Outline each Babesia divergens-infected red blood cell.
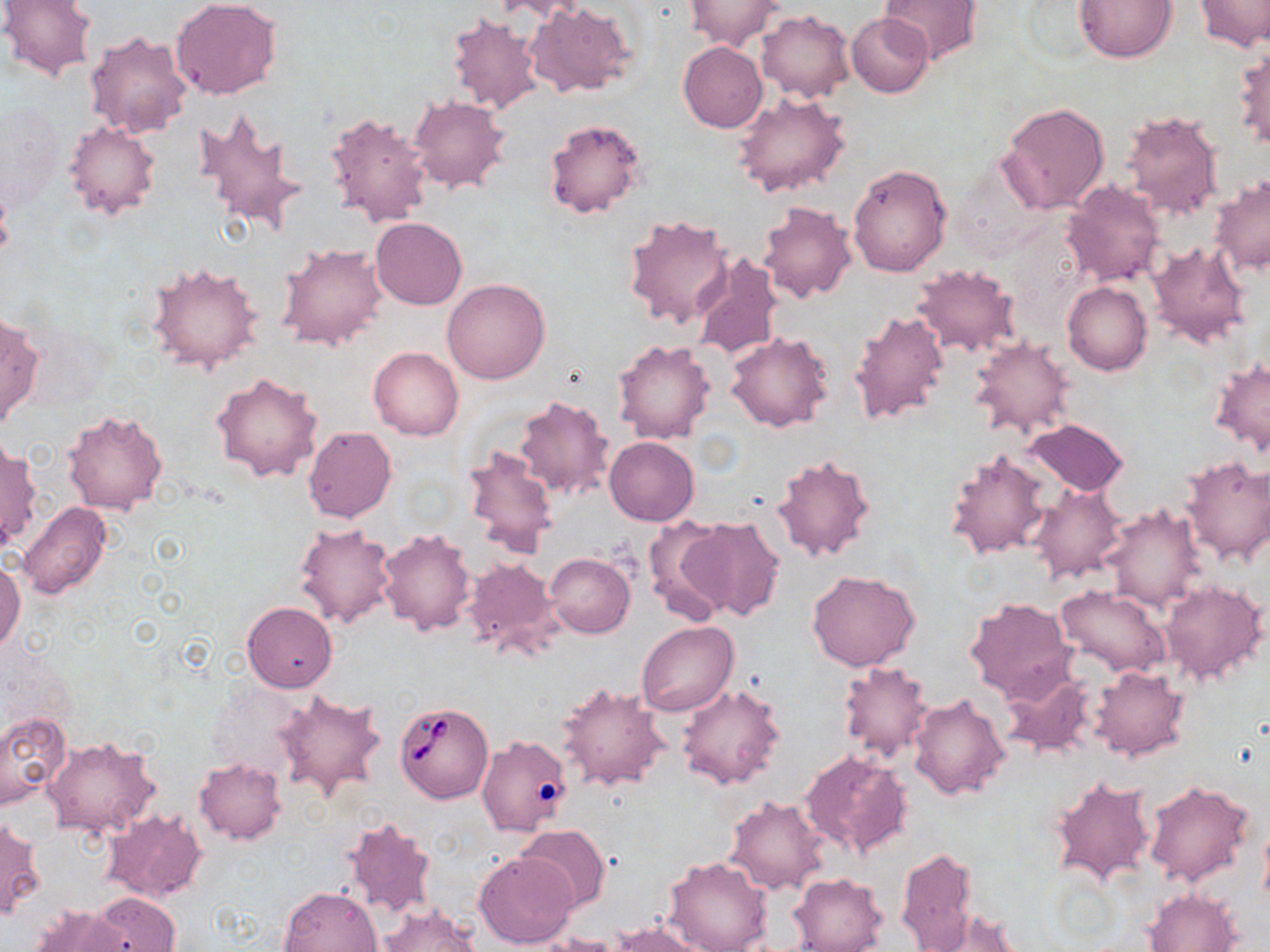

Approximate bounding boxes as [x1, y1, x2, y2] in pixels.
Babesia divergens-infected red blood cells: [394, 701, 494, 804].

Summary:
  - Uninfected red blood cell locations: [0, 0, 97, 81], [170, 0, 282, 101], [493, 0, 594, 22], [878, 0, 982, 66], [1075, 0, 1178, 63], [1195, 0, 1269, 51], [684, 1, 785, 51], [525, 3, 636, 98], [756, 10, 854, 103], [447, 13, 543, 115], [846, 13, 934, 99], [85, 32, 192, 140], [677, 41, 768, 132], [1232, 42, 1269, 151], [733, 92, 851, 197], [409, 95, 510, 193], [999, 102, 1111, 213], [194, 107, 306, 232], [323, 109, 434, 229], [1119, 110, 1224, 221], [543, 116, 648, 220], [64, 120, 161, 220], [848, 164, 952, 277], [1210, 176, 1269, 277], [1060, 180, 1166, 287], [756, 200, 858, 303], [624, 213, 734, 330], [370, 217, 467, 310], [1146, 241, 1252, 348], [278, 242, 387, 350], [691, 252, 784, 361], [147, 260, 264, 374], [910, 264, 1024, 358], [442, 278, 550, 384], [1063, 281, 1152, 375], [847, 307, 950, 427], [0, 314, 44, 431], [725, 332, 833, 431], [969, 337, 1076, 442], [612, 339, 714, 445], [369, 346, 464, 439], [1210, 357, 1270, 455], [212, 371, 323, 482], [513, 394, 615, 502], [62, 409, 168, 514], [1024, 418, 1129, 497], [303, 426, 397, 523], [605, 436, 699, 526], [1, 440, 40, 550], [463, 444, 561, 558], [944, 448, 1054, 560], [769, 452, 876, 562], [1180, 457, 1270, 566], [1026, 484, 1127, 584], [18, 502, 112, 601], [1101, 503, 1209, 612], [683, 515, 785, 623], [641, 516, 731, 624], [293, 524, 396, 629], [376, 527, 476, 636], [545, 553, 635, 638], [463, 556, 564, 659], [0, 559, 24, 654], [806, 569, 920, 672], [1160, 580, 1268, 684], [1058, 586, 1173, 677], [964, 596, 1077, 704], [242, 601, 338, 692], [638, 621, 737, 717], [838, 660, 933, 763], [1089, 665, 1190, 762], [999, 666, 1099, 760], [557, 681, 670, 791], [677, 683, 786, 790], [275, 689, 387, 803], [908, 692, 1010, 802], [0, 711, 71, 808], [476, 736, 573, 837], [43, 737, 160, 839], [799, 748, 913, 859], [194, 757, 287, 844], [1051, 776, 1157, 891], [1143, 779, 1256, 888], [723, 796, 829, 895], [99, 808, 208, 904], [341, 815, 438, 920], [1, 816, 44, 919], [1259, 820, 1270, 911], [516, 824, 612, 911], [897, 846, 979, 952], [474, 851, 578, 949], [662, 854, 773, 952], [788, 873, 887, 952], [280, 886, 382, 952], [1145, 888, 1242, 951], [92, 892, 180, 952], [31, 905, 132, 951], [375, 905, 480, 952], [924, 909, 1023, 952], [609, 922, 712, 952], [536, 933, 624, 952]
  - Slide-level diagnosis: Babesia divergens
  - Magnification: 1000x
  - Field of view: single
  - Image size: 1270×952 pixels
  - Stain: May-Grünwald-Giemsa
  - Preparation: thin blood smear
  - Modality: optical microscopy